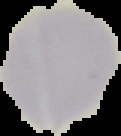

preparation: thin blood film
image_size: 121×136 pixels
result: no malaria parasites seen
image_type: cell region segmented out of the field of view; surrounding area masked to black